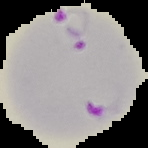

Summary:
  - Preparation: thin blood film
  - Image size: 148×148 pixels
  - Malaria status: parasitized
  - Image type: cell region segmented out of the field of view; surrounding area masked to black